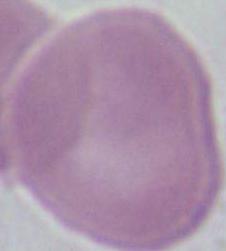
Summary:
  - Modality: micrograph
  - Identification: erythrocyte
  - Magnification: 1000x